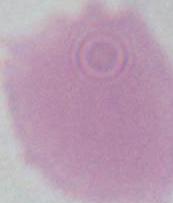
Summary:
  - Magnification: 1000x
  - Identification: red blood cell
  - Modality: photomicrograph